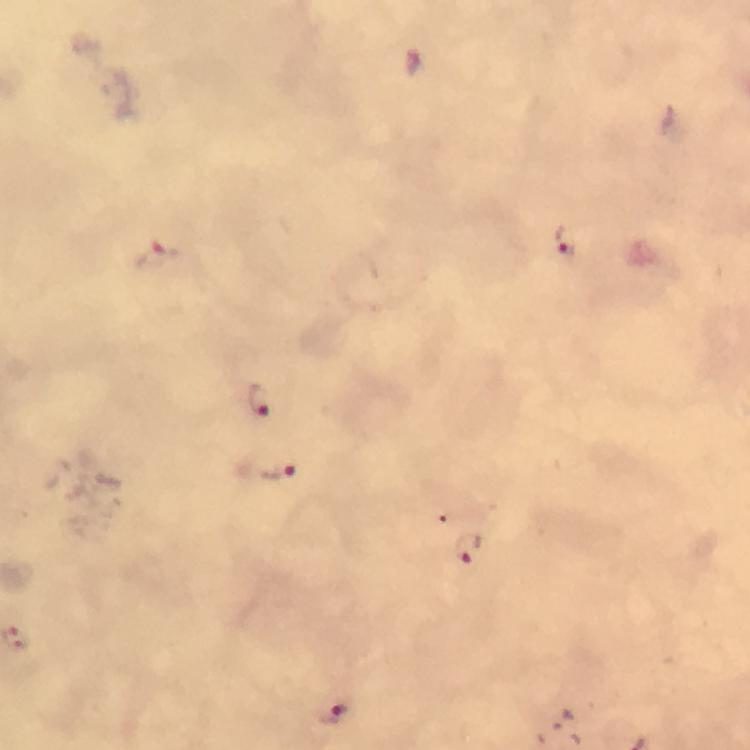
Approximate centers as (x, y) in pixels. Malaria parasite locations: (564, 240), (157, 256), (260, 399), (277, 473), (470, 549), (334, 712). Immersion oil applied. Thick blood film. Giemsa-stained preparation. A crop from one field of view. Image is 750×750 pixels. 100x magnification. From a malaria diagnostic workup. Smartphone photograph taken through a microscope.